Outline each Trypanosoma brucei.
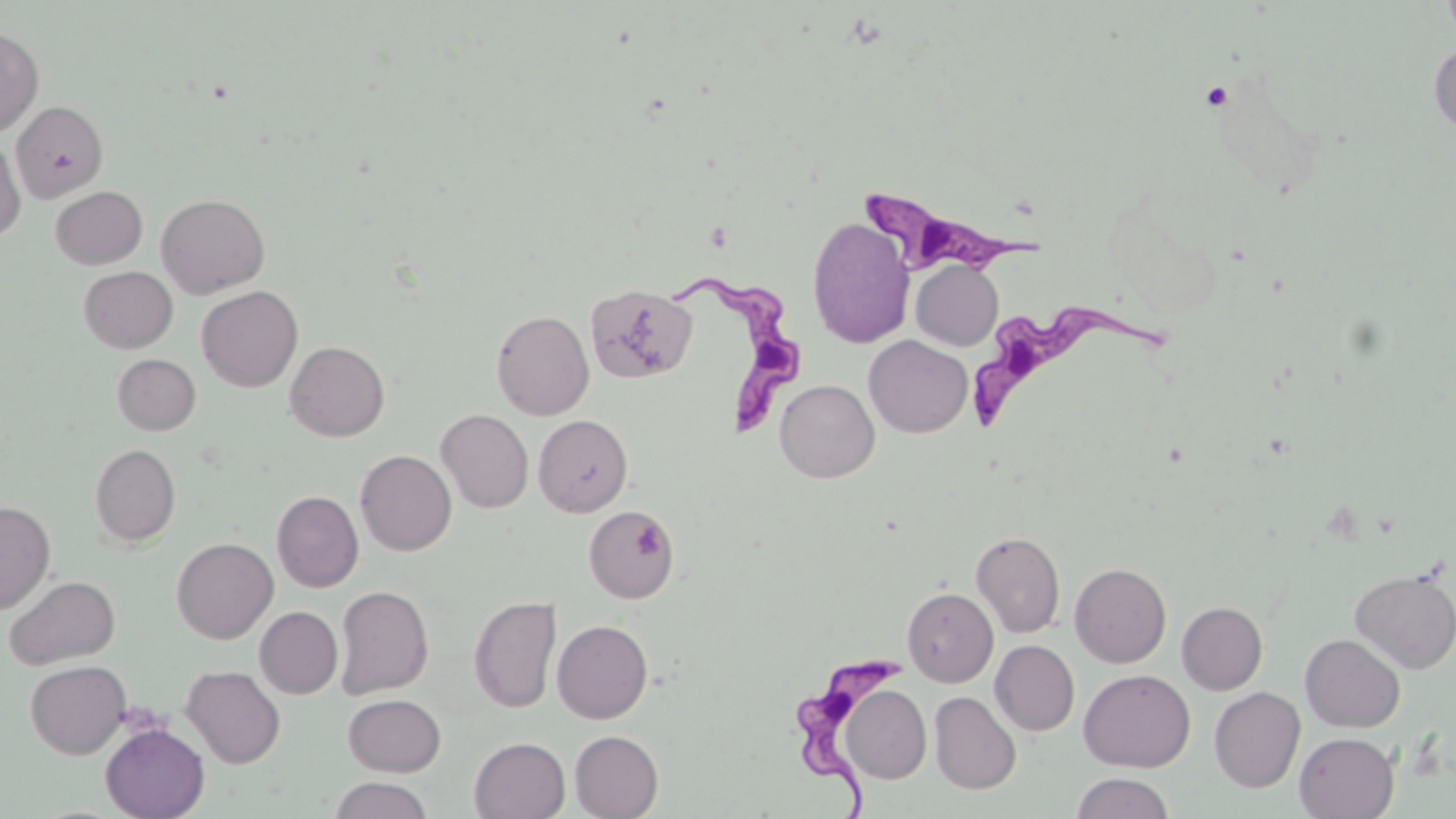
Approximate bounding boxes as (x1,y1)-(x2,y2) corner pairs in pixels.
Trypanosoma brucei: (865,185)-(1042,281), (676,270)-(812,436), (972,298)-(1180,424), (794,655)-(914,819).

slide-level diagnosis = Trypanosoma brucei
uninfected red blood cell locations = approximate bounding boxes as (x1,y1)-(x2,y2) corner pairs in pixels: (1441,0)-(1456,42), (0,26)-(43,138), (1429,41)-(1456,134), (11,100)-(108,202), (0,137)-(25,243), (50,186)-(147,269), (156,193)-(270,298), (806,216)-(915,349), (911,260)-(1003,350), (79,266)-(178,353), (585,283)-(697,384), (197,286)-(302,392), (491,309)-(594,420), (864,335)-(973,438), (285,341)-(389,441), (112,354)-(201,435), (775,379)-(879,482), (436,409)-(533,513), (533,415)-(632,516), (90,443)-(181,547), (355,450)-(456,556), (272,490)-(363,592), (0,500)-(55,615), (583,505)-(679,604), (970,530)-(1065,638), (172,537)-(278,644), (1069,562)-(1171,668), (1350,567)-(1456,673), (5,575)-(120,669), (335,585)-(433,699), (902,587)-(998,687), (469,595)-(562,713), (1177,602)-(1267,694), (255,606)-(343,698), (552,619)-(653,723), (1300,633)-(1406,732), (990,640)-(1079,735), (25,660)-(131,758), (181,665)-(285,769), (1078,669)-(1196,772), (839,685)-(932,784), (1209,687)-(1305,792), (929,691)-(1021,794), (343,694)-(446,776), (100,723)-(210,819), (570,730)-(664,819), (1294,732)-(1399,818), (469,736)-(570,819), (1070,772)-(1175,818), (328,776)-(434,819)
stain = May-Grünwald-Giemsa
preparation = thin blood film
field of view = single
image size = 1456×819 pixels
magnification = 1000x
modality = light microscopy